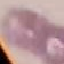

Result: no malaria parasites detected. Thin blood film. Giemsa-stained preparation. Automatically extracted cell patch, resized to 64 × 64 pixels. Acquired by smartphone through the microscope eyepiece.